Report the malaria status of this cell.
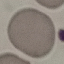

Uninfected.

Summary:
  - Stain: Giemsa
  - Capture: smartphone camera at the microscope eyepiece
  - Image type: cell patch, automatically extracted from a larger field of view and resized to 64 × 64 pixels
  - Preparation: thin blood film